Assess this cell for malaria.
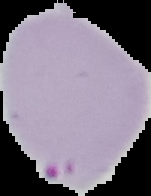
Parasitized.

Summary:
  - Image type: segmented cell region on a black background
  - Preparation: thin blood smear
  - Image size: 151×196 pixels